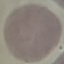 Result: no malaria parasites detected. Giemsa stain. Thin blood film. Automatically extracted cell patch, resized to 64 × 64 pixels. Photographed with a smartphone camera at the microscope eyepiece.